State the preparation type.
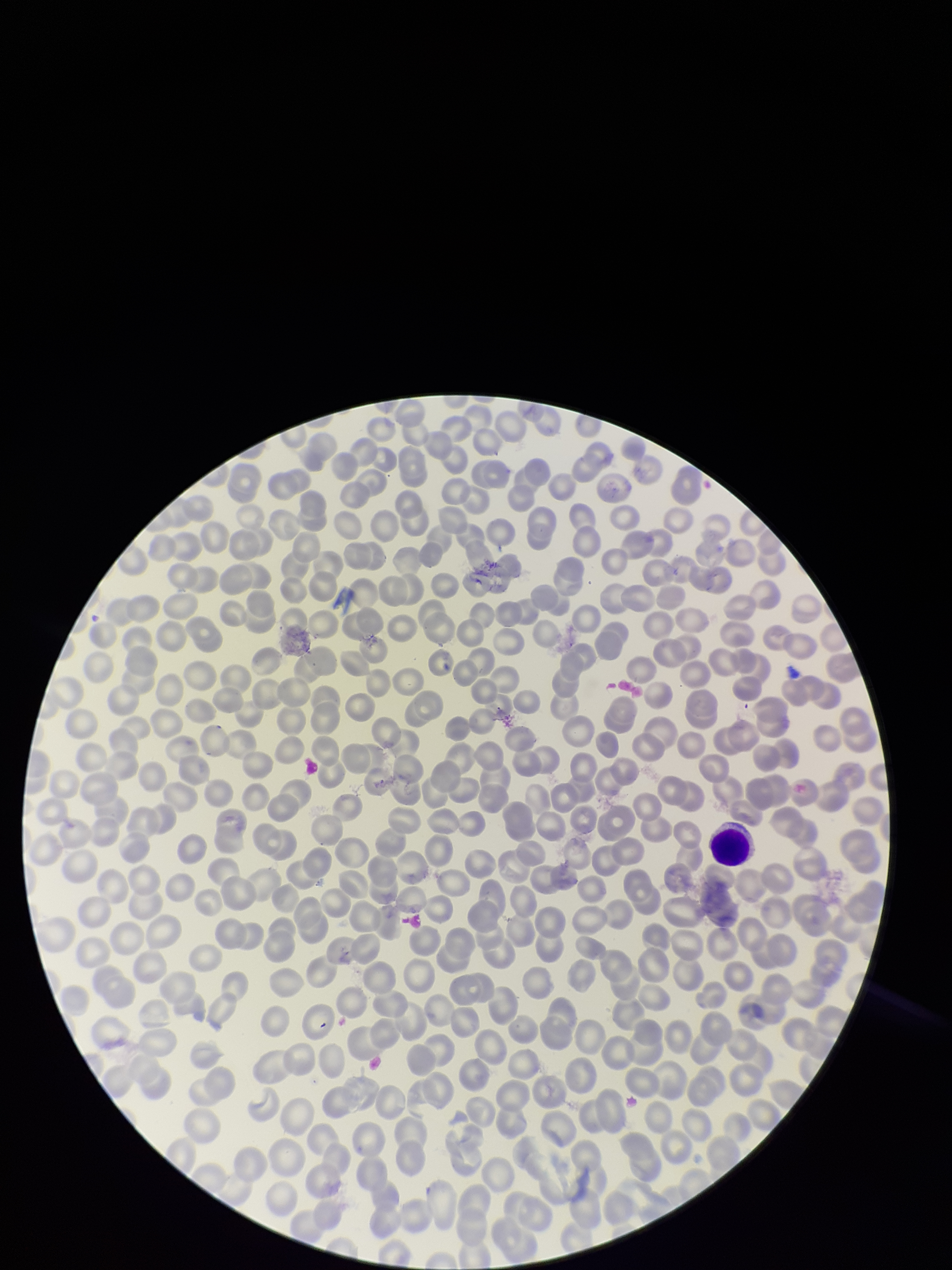
A thin smear.

patient_malaria_status: positive
capture: smartphone photograph through the microscope eyepiece
red_blood_cell_count: 318
field_of_view: one from this slide
image_size: 952×1270 pixels
parasitized_red_blood_cells: none seen
stain: Giemsa
parasitized_red_blood_cell_count: 0
species_reported_for_this_patient: Plasmodium falciparum